Identify the cell.
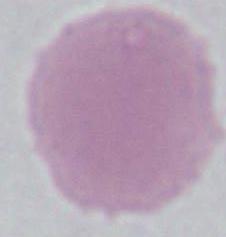

An erythrocyte.

Photomicrograph. Captured at 1000x magnification.